Report the malaria status of this cell.
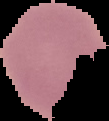

It is uninfected.

image_size: 109×121 pixels
preparation: thin blood smear
image_type: segmented cell region on a black background